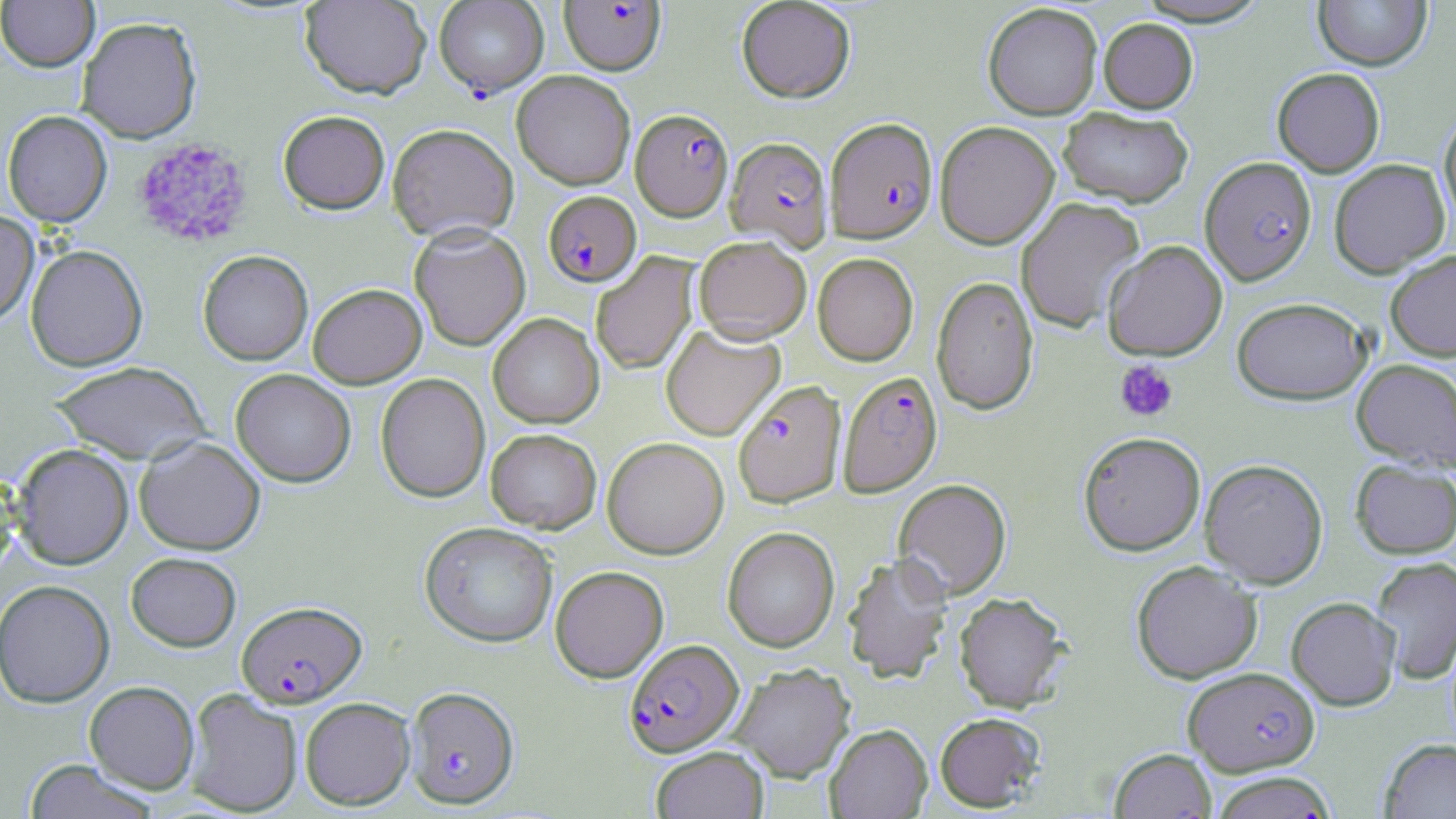

{
  "slide_level_diagnosis": "Plasmodium falciparum",
  "modality": "optical microscopy",
  "platelet_locations": "approximate bounding boxes as (x1,y1)-(x2,y2) corner pairs in pixels: (132,137)-(254,249), (1114,360)-(1178,422)",
  "magnification": "1000x",
  "uninfected_red_blood_cell_locations": "approximate bounding boxes as (x1,y1)-(x2,y2) corner pairs in pixels: (0,0)-(99,72), (300,0)-(431,99), (736,0)-(856,103), (1131,0)-(1274,26), (1313,0)-(1432,70), (982,2)-(1103,120), (76,16)-(202,143), (1098,18)-(1198,113), (1272,68)-(1385,177), (512,70)-(635,189), (1058,107)-(1193,207), (2,110)-(112,227), (278,110)-(390,213), (1439,112)-(1456,233), (934,120)-(1059,249), (387,123)-(519,243), (1329,159)-(1450,278), (1015,196)-(1146,333), (0,210)-(39,327), (410,224)-(530,351), (693,235)-(811,343), (1102,240)-(1228,360), (26,244)-(147,371), (198,250)-(313,365), (1385,250)-(1456,361), (813,252)-(919,366), (590,253)-(699,375), (931,276)-(1039,415), (308,283)-(426,388), (1231,297)-(1373,404), (488,313)-(603,428), (661,323)-(784,439), (1352,359)-(1456,471), (49,360)-(211,465), (231,369)-(355,487), (375,373)-(490,502), (485,428)-(601,533), (1078,431)-(1206,556), (135,436)-(265,555), (602,437)-(729,559), (12,444)-(133,569), (1351,458)-(1456,559), (1200,459)-(1328,588), (0,464)-(19,579), (894,478)-(1012,600), (420,521)-(558,647), (722,526)-(839,652), (126,552)-(241,651), (842,552)-(953,684), (1370,556)-(1456,685), (1131,560)-(1263,683), (550,565)-(668,682), (0,579)-(115,708), (954,591)-(1070,712), (1286,596)-(1401,710), (731,663)-(855,781), (84,681)-(200,795), (184,689)-(303,816), (300,696)-(416,810), (934,712)-(1045,812), (825,723)-(932,818), (1379,739)-(1456,819), (651,745)-(769,818), (1110,747)-(1217,819), (23,760)-(160,818), (1208,771)-(1339,819)",
  "stain": "May-Grünwald-Giemsa",
  "field_of_view": "one of a larger specimen",
  "preparation": "thin blood smear",
  "plasmodium_falciparum_infected_red_blood_cell_locations": "approximate bounding boxes as (x1,y1)-(x2,y2) corner pairs in pixels: (434,0)-(548,97), (560,1)-(666,75), (631,109)-(733,220), (825,117)-(937,242), (726,136)-(833,252), (1200,156)-(1317,285), (543,191)-(641,286), (837,371)-(943,497), (732,380)-(846,507), (237,600)-(367,707), (624,638)-(744,757), (1183,666)-(1319,776), (405,686)-(520,808)",
  "image_size": "1456×819 pixels"
}